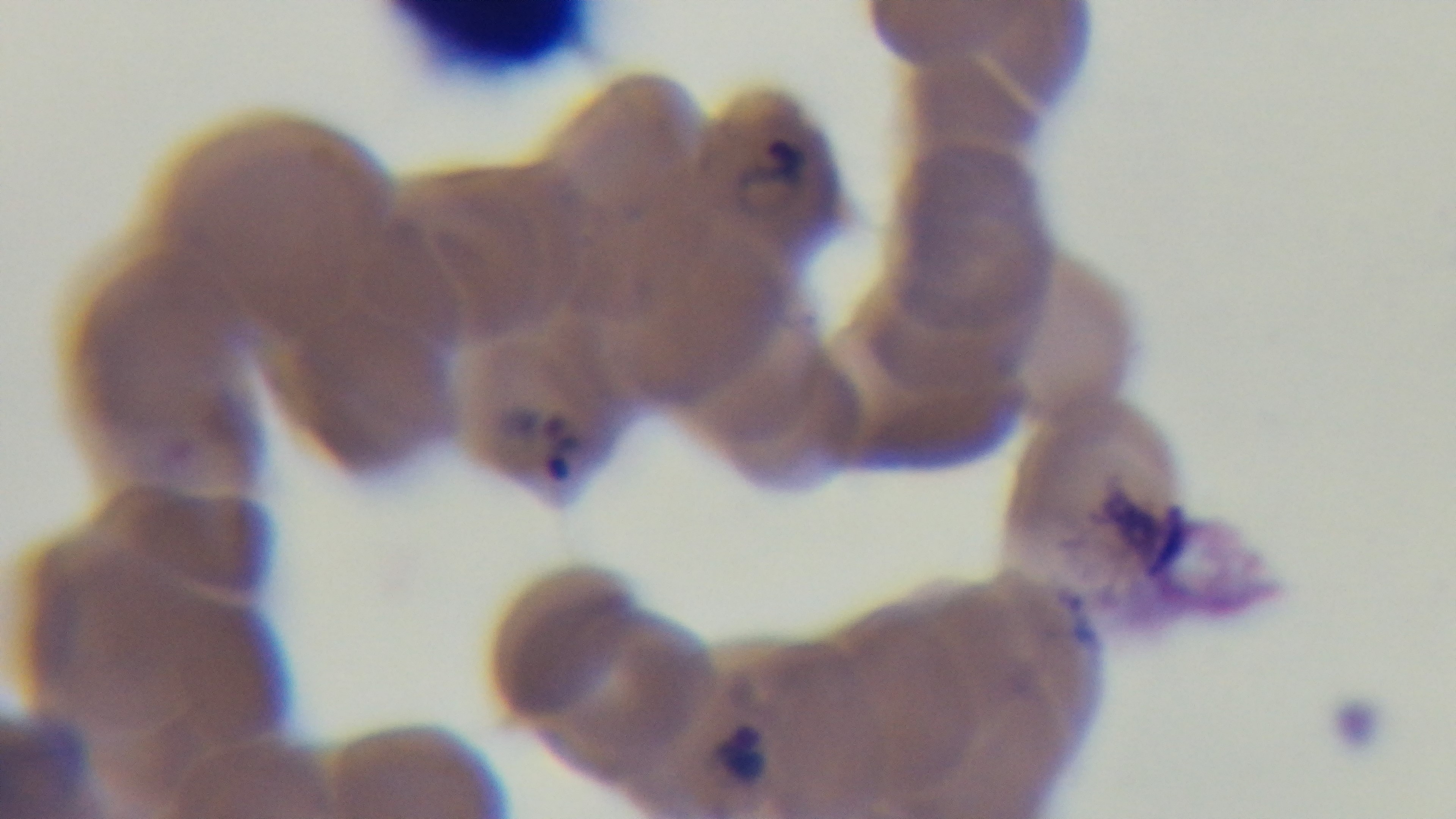

Summary:
  - Field of view: single
  - Objective: 100x oil immersion
  - Stain: Giemsa
  - Capture: mounted 4K digital camera
  - Malaria status: positive
  - Preparation: thin
  - Modality: light microscopy